State which cell type is depicted.
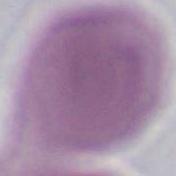

An erythrocyte.

1000x magnification. Photomicrograph.